Report the malaria status of this cell.
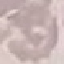
It is uninfected.

preparation = thin blood smear
stain = Giemsa
capture = smartphone camera at the microscope eyepiece
image type = automatically extracted cell patch, resized to 64 × 64 pixels